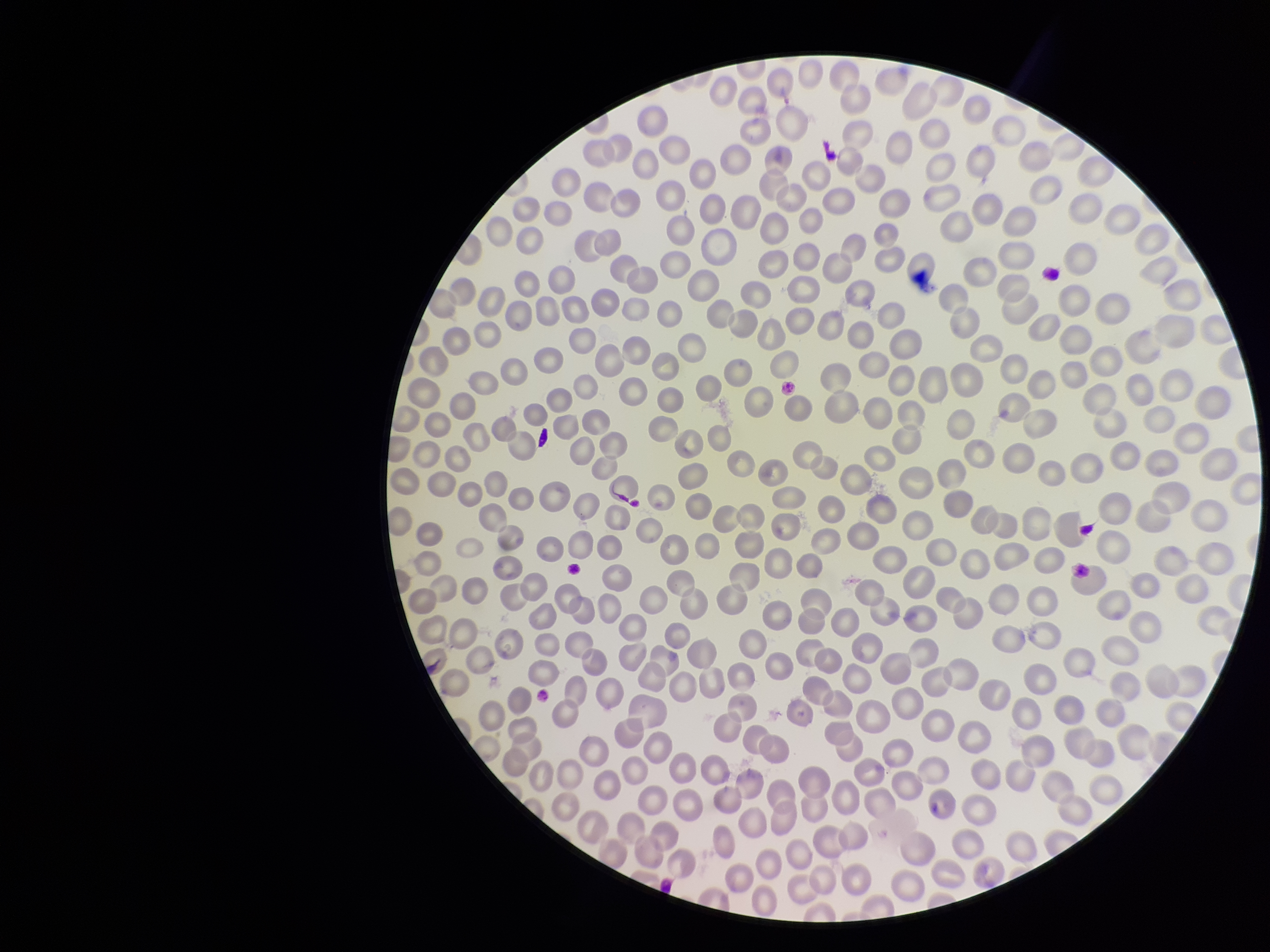

parasitized red blood cell count = 0
red blood cell count = 346
parasitized red blood cells = none identified
species reported for this patient = Plasmodium falciparum
patient malaria status = infected
image size = 1270×952 pixels
stain = Giemsa
preparation = thin blood smear
field of view = one from this slide
capture = smartphone photograph through the microscope eyepiece